Outline each Plasmodium ovale-infected red blood cell.
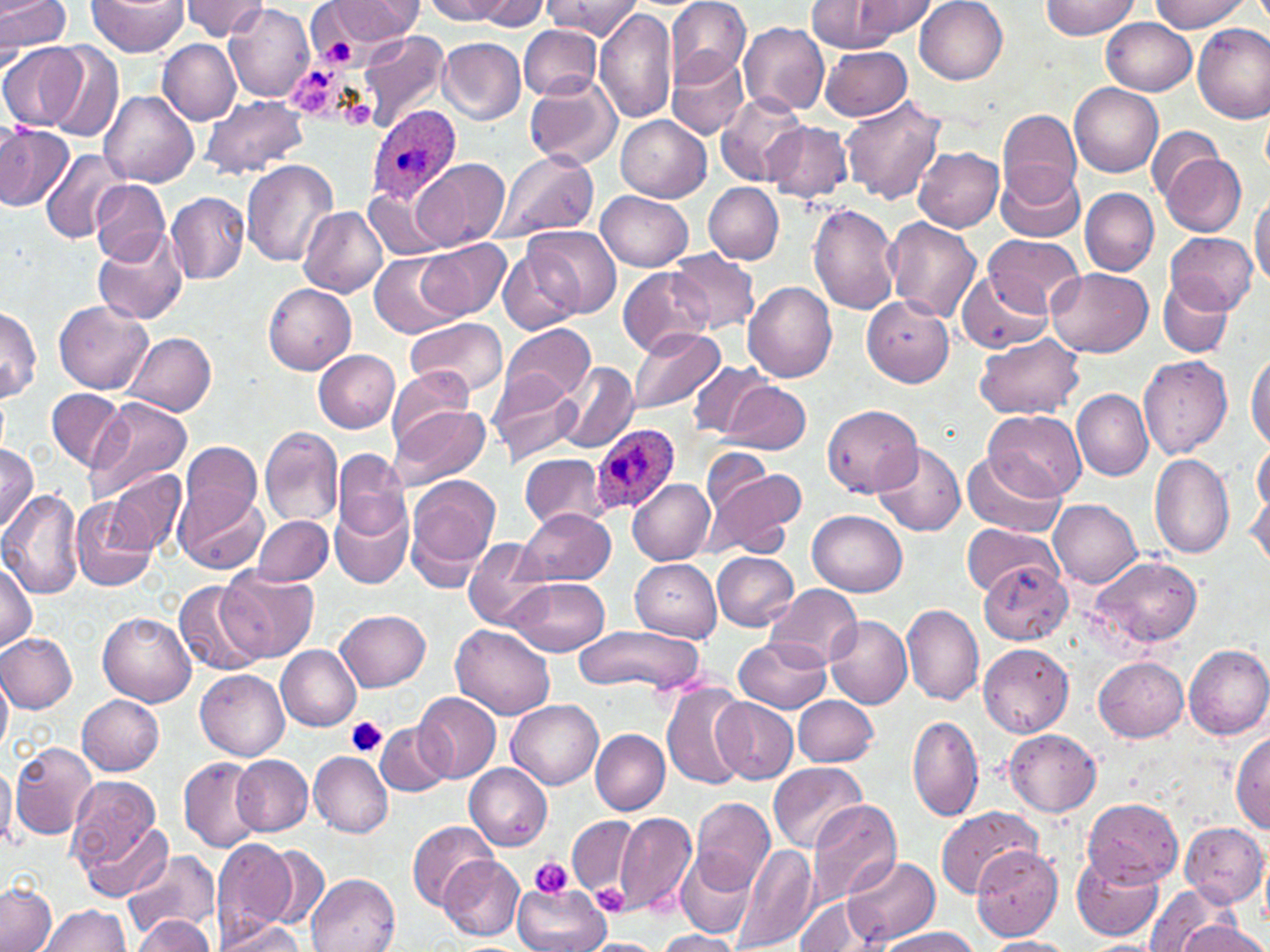
Approximate bounding boxes as named x1/y1/x2/y2 corners in pixels.
Plasmodium ovale-infected red blood cells: (x1=365, y1=105, x2=460, y2=203), (x1=592, y1=423, x2=679, y2=515).

slide-level diagnosis = Plasmodium ovale
preparation = thin blood film
platelet locations = approximate bounding boxes as named x1/y1/x2/y2 corners in pixels: (x1=314, y1=21, x2=358, y2=71), (x1=345, y1=716, x2=388, y2=758), (x1=529, y1=855, x2=574, y2=898), (x1=593, y1=883, x2=633, y2=916)
uninfected red blood cell locations = approximate bounding boxes as named x1/y1/x2/y2 corners in pixels: (x1=0, y1=0, x2=72, y2=60), (x1=86, y1=0, x2=188, y2=56), (x1=178, y1=0, x2=272, y2=41), (x1=327, y1=0, x2=418, y2=42), (x1=426, y1=0, x2=512, y2=22), (x1=476, y1=0, x2=547, y2=30), (x1=545, y1=0, x2=638, y2=41), (x1=666, y1=0, x2=753, y2=85), (x1=847, y1=0, x2=936, y2=42), (x1=1040, y1=0, x2=1138, y2=38), (x1=1149, y1=0, x2=1250, y2=33), (x1=808, y1=1, x2=908, y2=52), (x1=915, y1=1, x2=1007, y2=84), (x1=222, y1=2, x2=314, y2=103), (x1=594, y1=9, x2=678, y2=124), (x1=1102, y1=19, x2=1196, y2=96), (x1=739, y1=22, x2=829, y2=115), (x1=519, y1=24, x2=602, y2=99), (x1=1193, y1=24, x2=1270, y2=122), (x1=356, y1=30, x2=449, y2=131), (x1=438, y1=38, x2=526, y2=126), (x1=158, y1=40, x2=241, y2=126), (x1=1, y1=41, x2=86, y2=131), (x1=44, y1=43, x2=123, y2=143), (x1=820, y1=46, x2=913, y2=121), (x1=667, y1=51, x2=749, y2=139), (x1=524, y1=76, x2=622, y2=170), (x1=1070, y1=83, x2=1163, y2=178), (x1=101, y1=91, x2=199, y2=186), (x1=715, y1=91, x2=807, y2=186), (x1=200, y1=95, x2=309, y2=179), (x1=841, y1=96, x2=947, y2=205), (x1=998, y1=108, x2=1082, y2=204), (x1=616, y1=115, x2=712, y2=200), (x1=764, y1=121, x2=851, y2=203), (x1=0, y1=125, x2=74, y2=211), (x1=1148, y1=125, x2=1225, y2=204), (x1=912, y1=145, x2=1005, y2=232), (x1=40, y1=149, x2=129, y2=244), (x1=491, y1=149, x2=600, y2=243), (x1=1160, y1=154, x2=1246, y2=235), (x1=416, y1=158, x2=509, y2=250), (x1=242, y1=159, x2=338, y2=267), (x1=996, y1=162, x2=1083, y2=243), (x1=90, y1=179, x2=168, y2=265), (x1=704, y1=182, x2=784, y2=264), (x1=364, y1=186, x2=449, y2=260), (x1=1079, y1=187, x2=1159, y2=275), (x1=598, y1=191, x2=693, y2=271), (x1=167, y1=192, x2=249, y2=284), (x1=1250, y1=192, x2=1270, y2=288), (x1=806, y1=203, x2=900, y2=315), (x1=298, y1=205, x2=388, y2=297), (x1=884, y1=218, x2=982, y2=322), (x1=525, y1=224, x2=622, y2=319), (x1=91, y1=225, x2=188, y2=325), (x1=1165, y1=230, x2=1258, y2=314), (x1=984, y1=233, x2=1084, y2=313), (x1=418, y1=238, x2=511, y2=320), (x1=496, y1=246, x2=584, y2=335), (x1=670, y1=249, x2=759, y2=334), (x1=369, y1=252, x2=460, y2=339), (x1=619, y1=266, x2=713, y2=359), (x1=1047, y1=267, x2=1154, y2=357), (x1=956, y1=272, x2=1053, y2=352), (x1=1158, y1=279, x2=1233, y2=356), (x1=262, y1=282, x2=356, y2=375), (x1=742, y1=282, x2=838, y2=383), (x1=862, y1=295, x2=954, y2=387), (x1=54, y1=298, x2=153, y2=393), (x1=0, y1=305, x2=42, y2=402), (x1=405, y1=317, x2=508, y2=398), (x1=502, y1=322, x2=596, y2=403), (x1=628, y1=327, x2=725, y2=416), (x1=127, y1=331, x2=216, y2=417), (x1=973, y1=333, x2=1084, y2=419), (x1=313, y1=348, x2=399, y2=432), (x1=1246, y1=350, x2=1270, y2=451), (x1=1139, y1=353, x2=1233, y2=458), (x1=555, y1=361, x2=638, y2=451), (x1=690, y1=362, x2=772, y2=439), (x1=386, y1=369, x2=477, y2=445), (x1=490, y1=372, x2=582, y2=467), (x1=721, y1=380, x2=812, y2=455), (x1=46, y1=389, x2=127, y2=470), (x1=1074, y1=389, x2=1152, y2=480), (x1=87, y1=397, x2=193, y2=506), (x1=389, y1=402, x2=492, y2=490), (x1=822, y1=404, x2=922, y2=497), (x1=984, y1=408, x2=1085, y2=502), (x1=260, y1=428, x2=344, y2=527), (x1=873, y1=440, x2=967, y2=536), (x1=179, y1=441, x2=264, y2=526), (x1=0, y1=442, x2=38, y2=533), (x1=1252, y1=442, x2=1269, y2=522), (x1=703, y1=446, x2=771, y2=513), (x1=963, y1=449, x2=1062, y2=538), (x1=332, y1=450, x2=411, y2=539), (x1=520, y1=453, x2=609, y2=528), (x1=1149, y1=453, x2=1235, y2=560), (x1=104, y1=468, x2=187, y2=555), (x1=709, y1=468, x2=805, y2=560), (x1=406, y1=473, x2=502, y2=577), (x1=1248, y1=473, x2=1270, y2=573), (x1=628, y1=477, x2=715, y2=564), (x1=173, y1=485, x2=267, y2=574), (x1=0, y1=489, x2=84, y2=601), (x1=70, y1=496, x2=159, y2=592), (x1=1049, y1=499, x2=1143, y2=588), (x1=330, y1=502, x2=414, y2=590), (x1=520, y1=507, x2=615, y2=585), (x1=808, y1=510, x2=907, y2=597), (x1=253, y1=515, x2=333, y2=585), (x1=961, y1=522, x2=1064, y2=594), (x1=463, y1=537, x2=551, y2=629), (x1=712, y1=551, x2=798, y2=632), (x1=0, y1=555, x2=38, y2=651), (x1=1087, y1=555, x2=1204, y2=650), (x1=628, y1=557, x2=722, y2=641), (x1=979, y1=563, x2=1071, y2=644), (x1=217, y1=566, x2=320, y2=662), (x1=510, y1=577, x2=609, y2=657), (x1=174, y1=580, x2=264, y2=674), (x1=765, y1=584, x2=863, y2=670), (x1=902, y1=604, x2=984, y2=707), (x1=335, y1=609, x2=431, y2=691), (x1=98, y1=611, x2=198, y2=706), (x1=824, y1=615, x2=912, y2=708), (x1=452, y1=624, x2=555, y2=719), (x1=574, y1=624, x2=703, y2=693), (x1=0, y1=633, x2=78, y2=712), (x1=734, y1=637, x2=830, y2=713), (x1=978, y1=643, x2=1074, y2=737), (x1=276, y1=644, x2=363, y2=730), (x1=1183, y1=644, x2=1270, y2=740), (x1=1093, y1=657, x2=1188, y2=742), (x1=0, y1=667, x2=12, y2=755), (x1=196, y1=669, x2=290, y2=761), (x1=661, y1=683, x2=750, y2=789), (x1=412, y1=691, x2=501, y2=783), (x1=77, y1=695, x2=165, y2=775), (x1=791, y1=695, x2=879, y2=767), (x1=713, y1=697, x2=799, y2=784), (x1=507, y1=700, x2=602, y2=788), (x1=907, y1=715, x2=983, y2=822), (x1=375, y1=722, x2=454, y2=797), (x1=1004, y1=729, x2=1102, y2=815), (x1=591, y1=730, x2=669, y2=814), (x1=1231, y1=730, x2=1270, y2=832), (x1=10, y1=741, x2=97, y2=840), (x1=309, y1=750, x2=394, y2=838), (x1=232, y1=755, x2=313, y2=836), (x1=178, y1=757, x2=266, y2=852), (x1=769, y1=762, x2=867, y2=852), (x1=465, y1=765, x2=553, y2=850), (x1=64, y1=773, x2=167, y2=884), (x1=689, y1=796, x2=775, y2=891), (x1=1083, y1=797, x2=1183, y2=887), (x1=806, y1=799, x2=901, y2=909), (x1=935, y1=805, x2=1040, y2=898), (x1=615, y1=813, x2=696, y2=918), (x1=567, y1=815, x2=636, y2=897), (x1=79, y1=817, x2=170, y2=904), (x1=406, y1=819, x2=496, y2=910), (x1=1180, y1=822, x2=1268, y2=908), (x1=211, y1=839, x2=297, y2=942), (x1=259, y1=843, x2=331, y2=932), (x1=733, y1=844, x2=819, y2=952), (x1=971, y1=845, x2=1063, y2=941), (x1=123, y1=847, x2=221, y2=942), (x1=677, y1=847, x2=757, y2=939), (x1=1071, y1=853, x2=1164, y2=941), (x1=440, y1=855, x2=524, y2=941), (x1=843, y1=855, x2=939, y2=947), (x1=307, y1=873, x2=400, y2=952), (x1=0, y1=883, x2=57, y2=952), (x1=514, y1=884, x2=609, y2=952), (x1=1142, y1=886, x2=1236, y2=952), (x1=795, y1=896, x2=875, y2=952), (x1=37, y1=903, x2=131, y2=952), (x1=1172, y1=913, x2=1267, y2=952), (x1=128, y1=916, x2=215, y2=951), (x1=214, y1=920, x2=309, y2=951), (x1=877, y1=926, x2=983, y2=952), (x1=652, y1=929, x2=742, y2=951), (x1=981, y1=937, x2=1074, y2=952), (x1=581, y1=938, x2=666, y2=952)
field of view = single
stain = May-Grünwald-Giemsa
image size = 1270×952 pixels
magnification = 1000x
modality = optical microscopy